Identify the parasite.
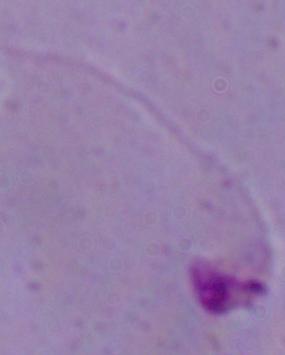
This is Leishmania.

Summary:
  - Magnification: 1000x
  - Modality: micrograph